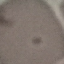 Malaria status: uninfected. Cell patch, automatically extracted from a larger field of view and resized to 64 × 64 pixels. Giemsa stain. Thin smear of blood. Acquired by smartphone through the microscope eyepiece.